Assess this cell for malaria.
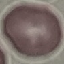

It is uninfected.

{
  "preparation": "thin smear",
  "capture": "smartphone camera at the microscope eyepiece",
  "stain": "Giemsa",
  "image_type": "cell patch, automatically extracted from a larger field of view and resized to 64 × 64 pixels"
}